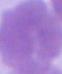
Summary:
  - Identification: red blood cell
  - Magnification: 1000x
  - Modality: photomicrograph